Locate every blood parasite and identify its species.
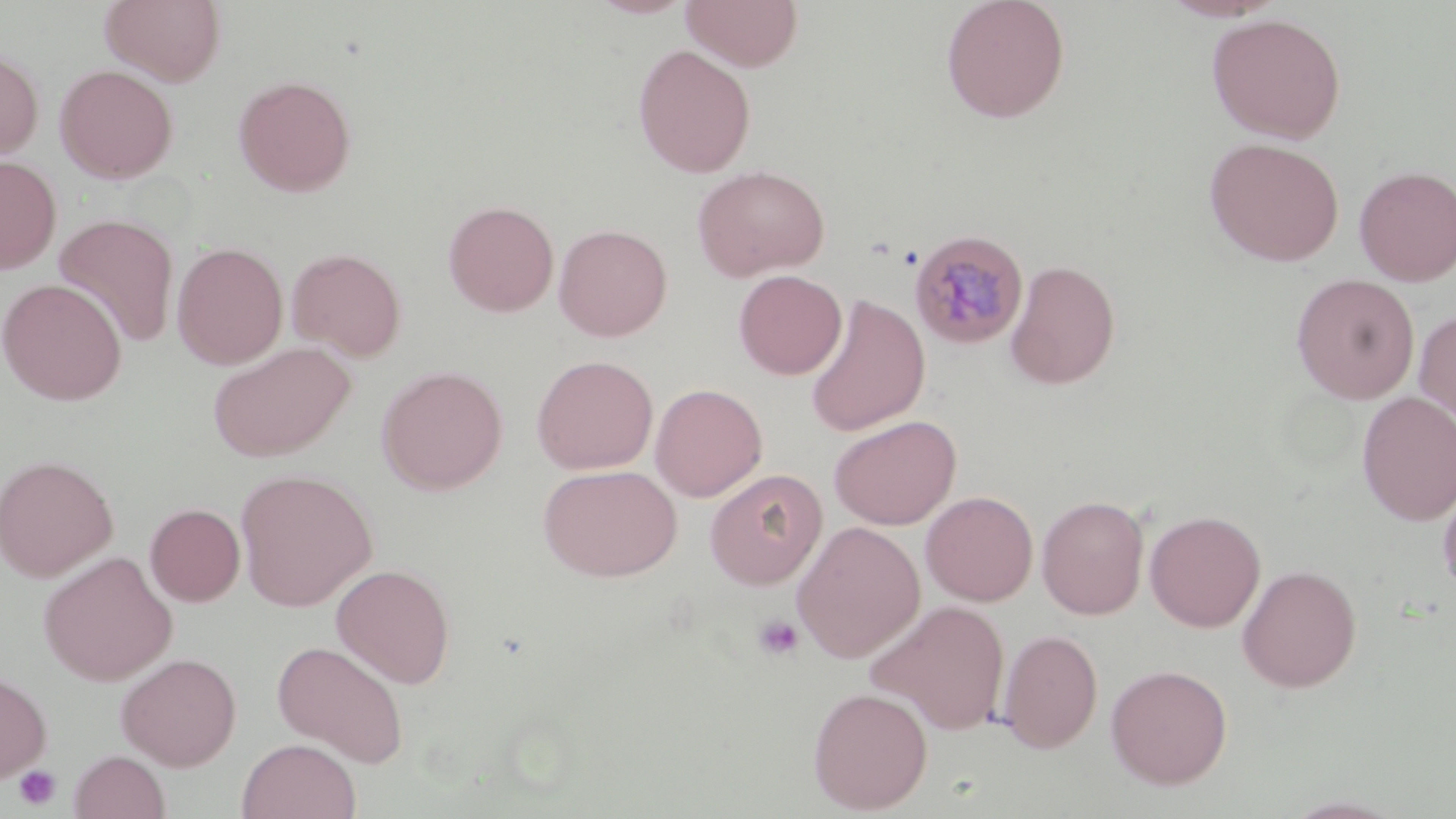

Approximate bounding boxes as named x1/y1/x2/y2 corners in pixels.
Plasmodium malariae-infected red blood cells: (x1=909, y1=229, x2=1029, y2=350).
No Plasmodium falciparum, Plasmodium ovale, Plasmodium vivax, Babesia divergens, or Trypanosoma brucei observed.

slide-level diagnosis = Plasmodium malariae
platelet locations = approximate bounding boxes as named x1/y1/x2/y2 corners in pixels: (x1=752, y1=614, x2=804, y2=661), (x1=13, y1=766, x2=62, y2=810)
field of view = one of a larger specimen
preparation = thin blood film
modality = optical microscopy
image size = 1456×819 pixels
magnification = 1000x
stain = May-Grünwald-Giemsa
uninfected red blood cell locations = approximate bounding boxes as named x1/y1/x2/y2 corners in pixels: (x1=99, y1=0, x2=226, y2=85), (x1=588, y1=0, x2=697, y2=18), (x1=681, y1=0, x2=803, y2=71), (x1=940, y1=0, x2=1070, y2=123), (x1=1206, y1=13, x2=1346, y2=143), (x1=633, y1=44, x2=756, y2=178), (x1=0, y1=48, x2=44, y2=163), (x1=55, y1=64, x2=178, y2=183), (x1=234, y1=75, x2=357, y2=197), (x1=1205, y1=137, x2=1344, y2=266), (x1=0, y1=155, x2=61, y2=275), (x1=692, y1=164, x2=830, y2=281), (x1=1353, y1=165, x2=1456, y2=287), (x1=443, y1=200, x2=559, y2=317), (x1=54, y1=214, x2=180, y2=348), (x1=554, y1=224, x2=673, y2=341), (x1=172, y1=241, x2=288, y2=369), (x1=286, y1=247, x2=407, y2=361), (x1=1005, y1=259, x2=1121, y2=390), (x1=733, y1=269, x2=847, y2=379), (x1=1291, y1=273, x2=1420, y2=403), (x1=0, y1=278, x2=127, y2=405), (x1=804, y1=295, x2=930, y2=437), (x1=1415, y1=308, x2=1456, y2=429), (x1=208, y1=341, x2=357, y2=462), (x1=531, y1=354, x2=658, y2=474), (x1=376, y1=365, x2=508, y2=494), (x1=650, y1=383, x2=768, y2=502), (x1=1356, y1=392, x2=1456, y2=526), (x1=828, y1=415, x2=961, y2=530), (x1=0, y1=454, x2=118, y2=581), (x1=538, y1=464, x2=682, y2=581), (x1=235, y1=468, x2=377, y2=612), (x1=704, y1=468, x2=827, y2=589), (x1=1438, y1=480, x2=1456, y2=600), (x1=920, y1=490, x2=1038, y2=606), (x1=1036, y1=495, x2=1150, y2=620), (x1=145, y1=503, x2=245, y2=606), (x1=1144, y1=509, x2=1266, y2=632), (x1=791, y1=521, x2=925, y2=662), (x1=38, y1=551, x2=178, y2=685), (x1=332, y1=563, x2=456, y2=689), (x1=1237, y1=564, x2=1362, y2=692), (x1=866, y1=600, x2=1011, y2=735), (x1=997, y1=628, x2=1103, y2=754), (x1=272, y1=640, x2=410, y2=766), (x1=116, y1=652, x2=241, y2=770), (x1=1105, y1=663, x2=1233, y2=789), (x1=0, y1=668, x2=52, y2=784), (x1=807, y1=686, x2=933, y2=814), (x1=237, y1=738, x2=361, y2=819), (x1=69, y1=750, x2=170, y2=819), (x1=1279, y1=796, x2=1409, y2=818)